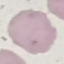
malaria status = uninfected
capture = smartphone camera at the microscope eyepiece
preparation = thin blood film
image type = automatically extracted cell patch, resized to 64 × 64 pixels
stain = Giemsa